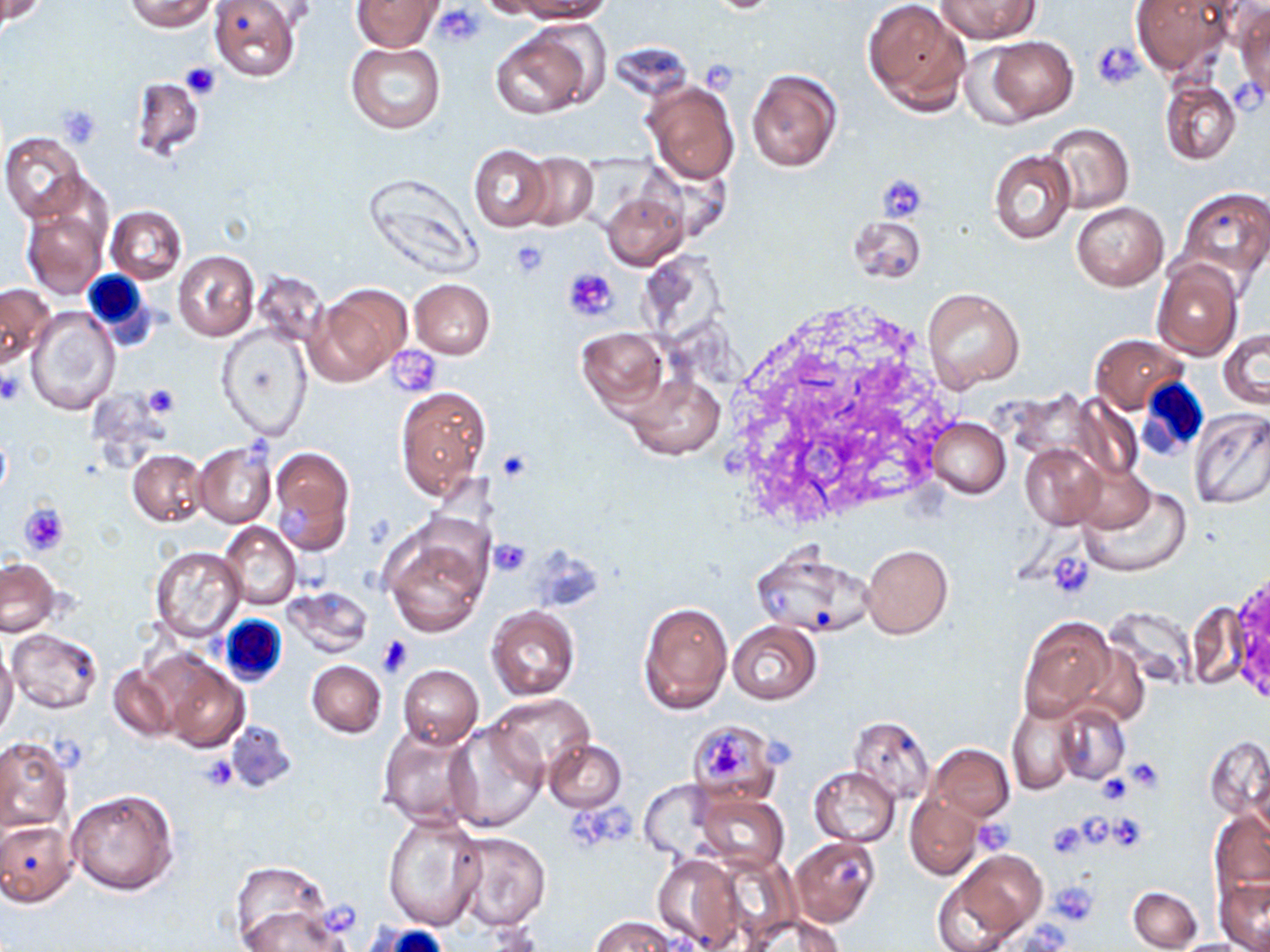

Approximate bounding boxes as [x1, y1, x2, y2] in pixels. Uninfected red blood cell locations: [1, 0, 44, 23], [127, 0, 215, 32], [209, 0, 300, 80], [353, 0, 443, 52], [476, 0, 559, 18], [516, 0, 614, 22], [861, 0, 971, 114], [936, 0, 1040, 43], [1130, 0, 1238, 77], [1233, 4, 1270, 105], [489, 20, 604, 120], [979, 34, 1079, 125], [346, 43, 445, 134], [746, 69, 843, 173], [129, 76, 205, 162], [643, 79, 741, 184], [1160, 80, 1241, 164], [1041, 122, 1133, 215], [2, 133, 87, 222], [468, 145, 552, 231], [988, 150, 1076, 245], [522, 153, 598, 228], [363, 174, 484, 280], [1175, 186, 1270, 284], [600, 192, 688, 270], [22, 200, 109, 298], [1071, 202, 1167, 290], [108, 205, 186, 283], [847, 216, 926, 284], [171, 249, 259, 342], [1151, 258, 1243, 361], [252, 272, 328, 345], [410, 279, 494, 359], [0, 283, 55, 367], [308, 284, 411, 384], [921, 287, 1026, 393], [26, 307, 120, 414], [217, 326, 311, 440], [1218, 327, 1269, 410], [577, 328, 669, 412], [1092, 335, 1187, 414], [622, 373, 724, 461], [396, 387, 489, 498], [1065, 393, 1147, 485], [1188, 407, 1270, 509], [928, 418, 1011, 499], [0, 430, 10, 500], [193, 443, 275, 528], [1021, 443, 1108, 530], [269, 448, 353, 552], [127, 450, 206, 526], [1072, 464, 1155, 536], [1078, 482, 1192, 578], [219, 522, 301, 609], [380, 523, 492, 636], [861, 544, 952, 639], [751, 545, 874, 638], [149, 546, 246, 640], [1, 558, 59, 637], [282, 585, 372, 658], [639, 601, 733, 715], [486, 608, 580, 701], [1019, 616, 1118, 720], [727, 621, 821, 704], [8, 629, 101, 713], [0, 644, 18, 742], [161, 654, 248, 752], [306, 661, 386, 737], [107, 663, 178, 742], [397, 665, 483, 749], [489, 695, 595, 779], [1007, 702, 1081, 794], [1054, 702, 1130, 786], [849, 717, 934, 804], [684, 721, 780, 805], [225, 722, 297, 793], [445, 723, 546, 832], [377, 725, 484, 832], [1205, 734, 1269, 825], [1, 738, 73, 832], [544, 738, 626, 813], [927, 743, 1013, 821], [810, 767, 899, 847], [638, 782, 723, 862], [67, 790, 178, 895], [696, 793, 788, 875], [904, 793, 983, 879], [1209, 811, 1270, 891], [382, 813, 487, 931], [0, 819, 77, 905], [450, 832, 551, 929], [789, 836, 880, 928], [653, 852, 746, 952], [939, 852, 1046, 946], [230, 860, 333, 950], [1216, 876, 1270, 952], [1128, 885, 1201, 951], [238, 899, 352, 952], [738, 912, 847, 952], [592, 917, 679, 952]. Platelet locations: [435, 4, 485, 47], [1092, 41, 1143, 89], [701, 58, 741, 91], [179, 63, 222, 99], [1233, 80, 1266, 117], [58, 103, 102, 145], [877, 173, 927, 224], [510, 238, 550, 276], [563, 267, 618, 322], [388, 347, 443, 396], [0, 370, 23, 404], [142, 384, 179, 416], [242, 435, 274, 472], [497, 450, 533, 481], [19, 503, 69, 555], [281, 503, 312, 542], [489, 539, 531, 576], [1047, 552, 1095, 598], [377, 634, 414, 677], [701, 729, 752, 780], [761, 736, 793, 769], [197, 756, 239, 792], [1123, 756, 1164, 793], [1098, 772, 1132, 806], [1106, 813, 1149, 852], [974, 818, 1015, 854], [1046, 820, 1088, 858], [834, 851, 864, 890], [1048, 882, 1099, 925]. White blood cell locations: [79, 269, 154, 341], [1138, 377, 1209, 458], [220, 615, 291, 694], [374, 923, 444, 952]. Slide-level diagnosis: no evidence of blood parasites. Captured at 1000x magnification. Single field of view. Thin blood film. Image is 1270×952 pixels. Light microscopy. May-Grünwald-Giemsa stain.